State the preparation type.
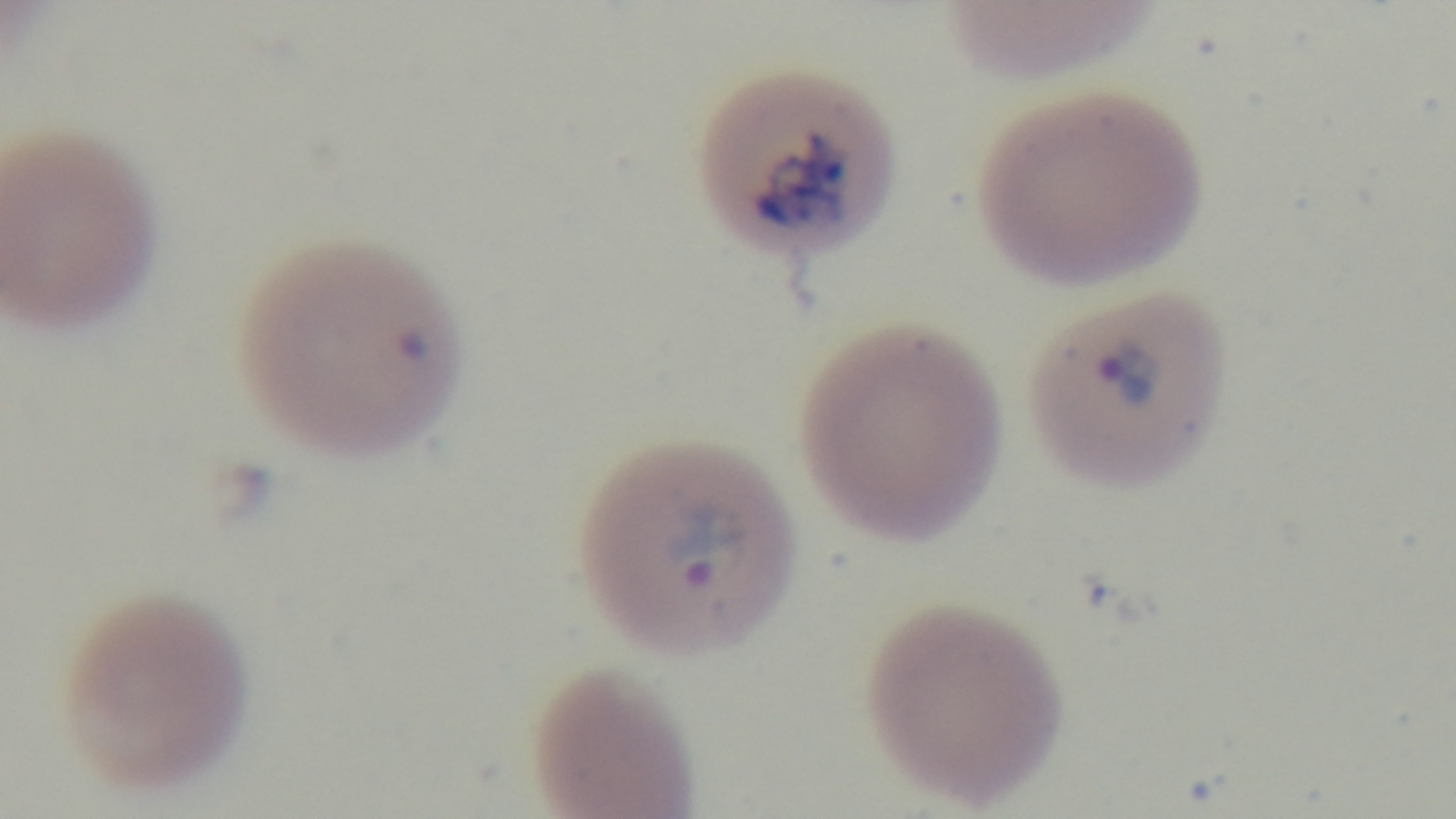

Thin.

Summary:
  - Modality: light microscopy
  - Objective: 100x oil immersion
  - Capture: mounted 4K digital camera
  - Field of view: one from the slide
  - Malaria status: infected
  - Stain: Giemsa